Point out each leukocyte.
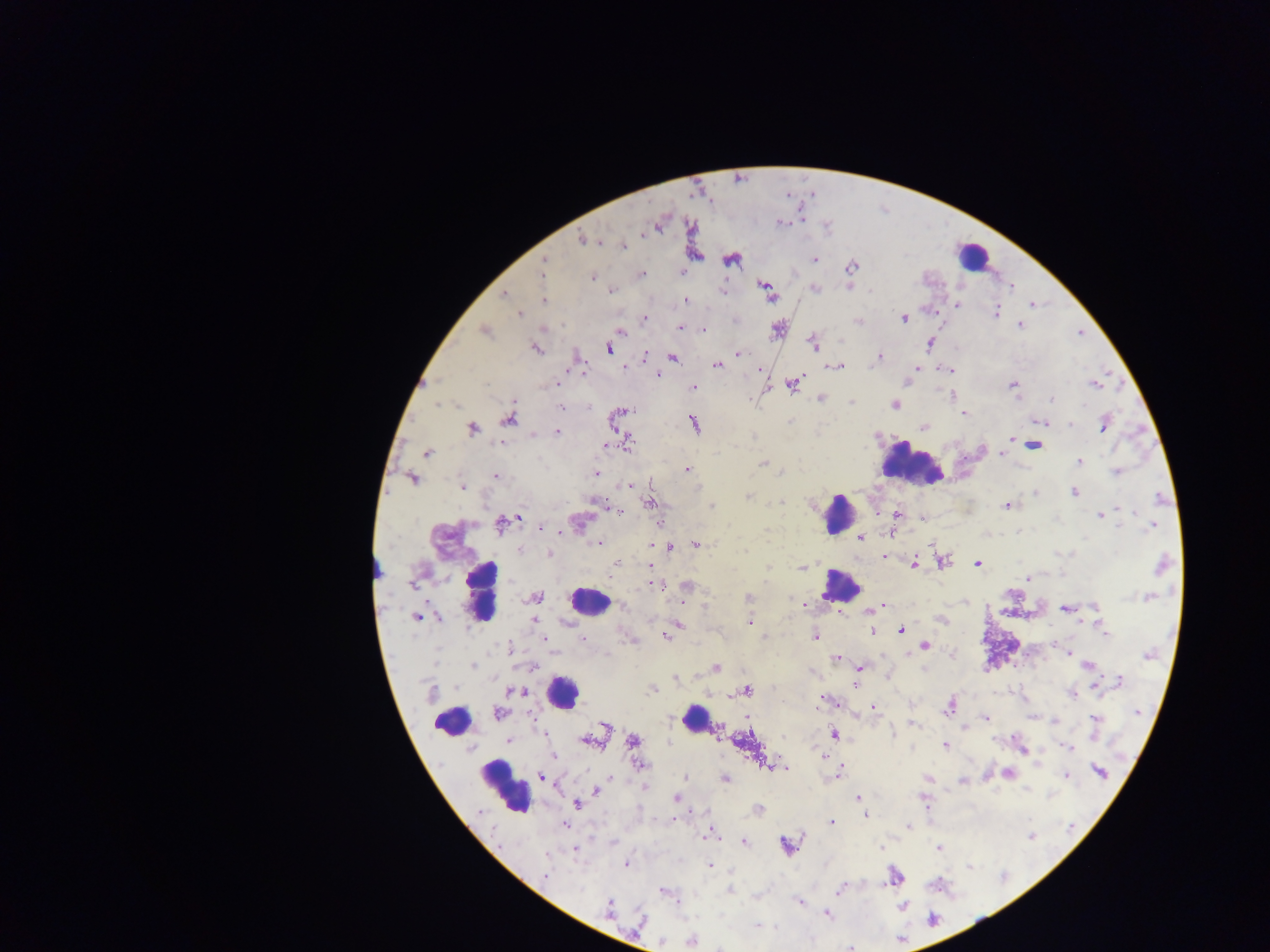
Approximate centers as {x, y} in pixels.
Leukocytes: {972, 256}, {910, 462}, {837, 514}, {842, 585}, {480, 592}, {589, 601}, {561, 692}, {694, 719}, {452, 720}, {504, 786}.

Summary:
  - Malaria parasite locations: {660, 222}, {780, 222}, {583, 239}, {622, 246}, {731, 259}, {814, 259}, {543, 264}, {850, 268}, {640, 274}, {593, 277}, {763, 283}, {850, 287}, {1012, 288}, {814, 289}, {610, 290}, {505, 294}, {771, 296}, {544, 300}, {685, 300}, {957, 304}, {1032, 304}, {995, 313}, {519, 314}, {644, 318}, {904, 318}, {858, 320}, {1019, 324}, {680, 327}, {701, 328}, {778, 328}, {484, 330}, {620, 332}, {929, 343}, {813, 344}, {535, 347}, {607, 348}, {737, 354}, {644, 356}, {878, 356}, {672, 358}, {716, 364}, {835, 366}, {624, 367}, {915, 367}, {759, 368}, {948, 370}, {582, 371}, {656, 374}, {792, 383}, {1013, 384}, {1094, 384}, {557, 385}, {693, 387}, {820, 399}, {1051, 399}, {852, 401}, {894, 405}, {561, 407}, {622, 411}, {965, 414}, {509, 419}, {1041, 422}, {694, 423}, {1103, 424}, {924, 427}, {471, 428}, {557, 431}, {1011, 439}, {1018, 440}, {627, 442}, {1033, 445}, {428, 452}, {1003, 454}, {1079, 462}, {763, 463}, {686, 469}, {1117, 472}, {596, 473}, {496, 475}, {413, 478}, {630, 485}, {462, 486}, {1073, 492}, {1036, 493}, {748, 497}, {596, 500}, {649, 502}, {781, 502}, {1006, 505}, {711, 506}, {1117, 509}, {618, 511}, {897, 515}, {1100, 515}, {518, 517}, {922, 517}, {510, 521}, {577, 522}, {501, 523}, {659, 523}, {1152, 526}, {540, 527}, {891, 533}, {861, 538}, {598, 543}, {695, 544}, {653, 545}, {668, 546}, {520, 550}, {550, 554}, {884, 557}, {940, 560}, {616, 563}, {914, 564}, {978, 564}, {649, 565}, {1161, 565}, {802, 566}, {1028, 578}, {658, 585}, {686, 586}, {534, 597}, {685, 597}, {1147, 597}, {748, 598}, {804, 605}, {883, 606}, {1066, 608}, {869, 611}, {417, 617}, {942, 619}, {534, 620}, {749, 622}, {679, 624}, {1102, 625}, {871, 630}, {901, 630}, {665, 635}, {814, 636}, {764, 637}, {544, 639}, {582, 639}, {630, 639}, {1053, 644}, {924, 645}, {509, 650}, {909, 653}, {1068, 653}, {836, 657}, {472, 665}, {1088, 665}, {715, 668}, {860, 668}, {676, 677}, {1118, 682}, {855, 684}, {1096, 685}, {653, 688}, {746, 690}, {515, 691}, {1072, 694}, {823, 699}, {836, 703}, {948, 706}, {872, 708}, {498, 712}, {748, 717}, {986, 717}, {1034, 717}, {1095, 718}, {1053, 720}, {910, 723}, {604, 725}, {965, 726}, {716, 730}, {834, 734}, {509, 741}, {588, 741}, {632, 741}, {945, 745}, {1067, 747}, {1022, 748}, {554, 755}, {822, 755}, {639, 765}, {767, 766}, {783, 768}, {787, 768}, {838, 772}, {1007, 772}, {1099, 772}, {1067, 775}, {542, 776}, {611, 777}, {686, 777}, {928, 778}, {725, 779}, {963, 781}, {645, 787}, {595, 791}, {677, 797}, {858, 798}, {924, 799}, {577, 804}, {758, 809}, {865, 814}, {672, 819}, {829, 821}, {565, 825}, {908, 826}, {711, 833}, {743, 842}, {787, 845}, {574, 848}, {881, 848}, {939, 848}, {626, 863}, {710, 866}, {894, 876}, {544, 877}, {841, 887}, {663, 891}, {729, 891}, {800, 902}, {902, 906}, {609, 908}, {826, 913}, {640, 921}, {757, 924}, {691, 939}, {661, 940}, {719, 946}
  - Country: Ghana
  - Field of view: single
  - Image size: 1270×952 pixels
  - Preparation: thick blood smear
  - Capture: mobile-phone photograph through a microscope